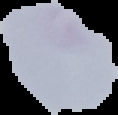
From a thin blood smear. Result: negative for Plasmodium parasites. Image is 118×115 pixels. Segmented cell region on a black background.